Classify this cell by malaria status.
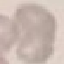
Uninfected.

preparation = thin blood film
capture = smartphone through the microscope eyepiece
stain = Giemsa
image type = automatically extracted cell patch, resized to 64 × 64 pixels